Comment on the morphology of the erythrocytes.
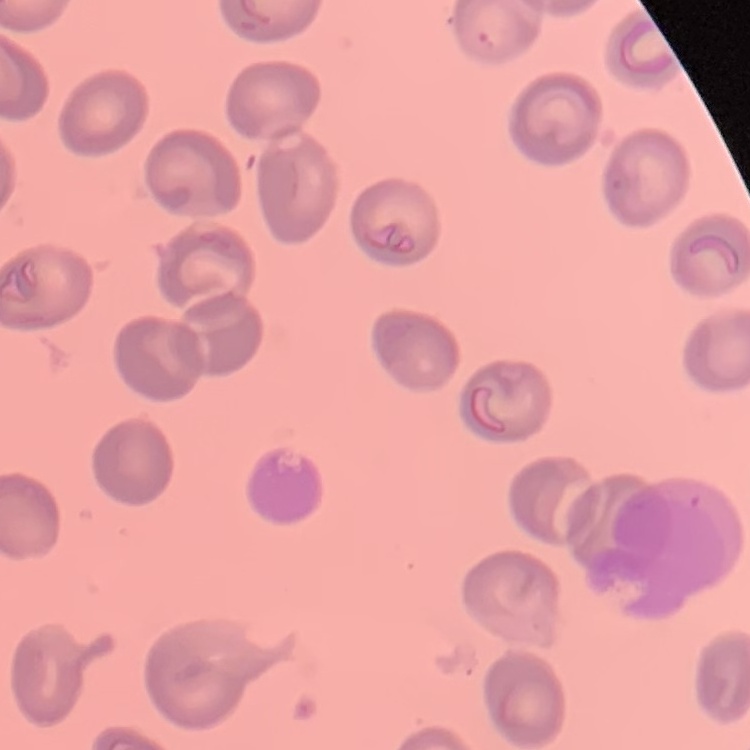

They show no rouleaux formation.

image type = square crop of a larger photomicrograph
preparation = thin peripheral smear
stain = Field's or Giemsa